Assess the morphology of the erythrocytes.
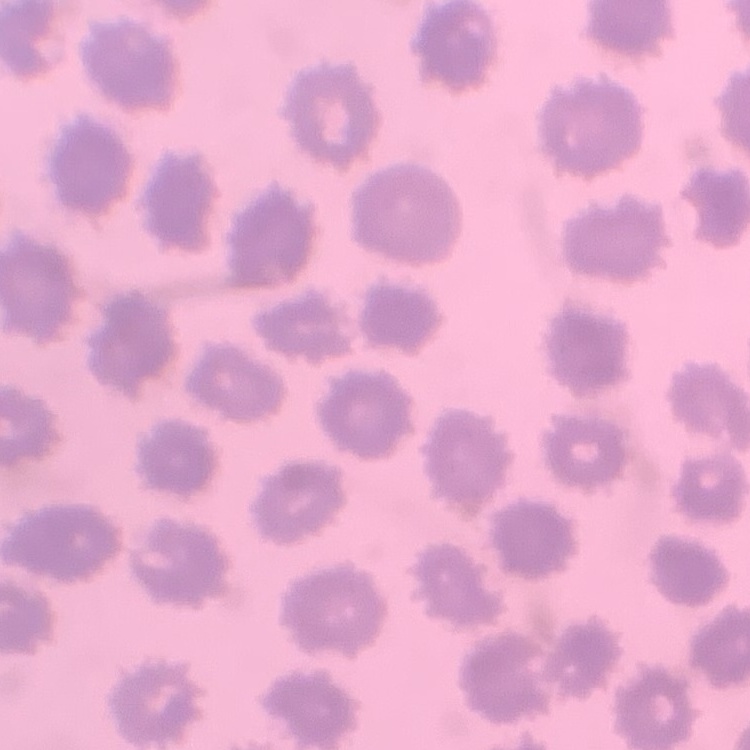
They show no rouleaux formation.

Summary:
  - Image type: one tile cut from a larger photomicrograph
  - Preparation: thin peripheral smear
  - Stain: Field's or Giemsa